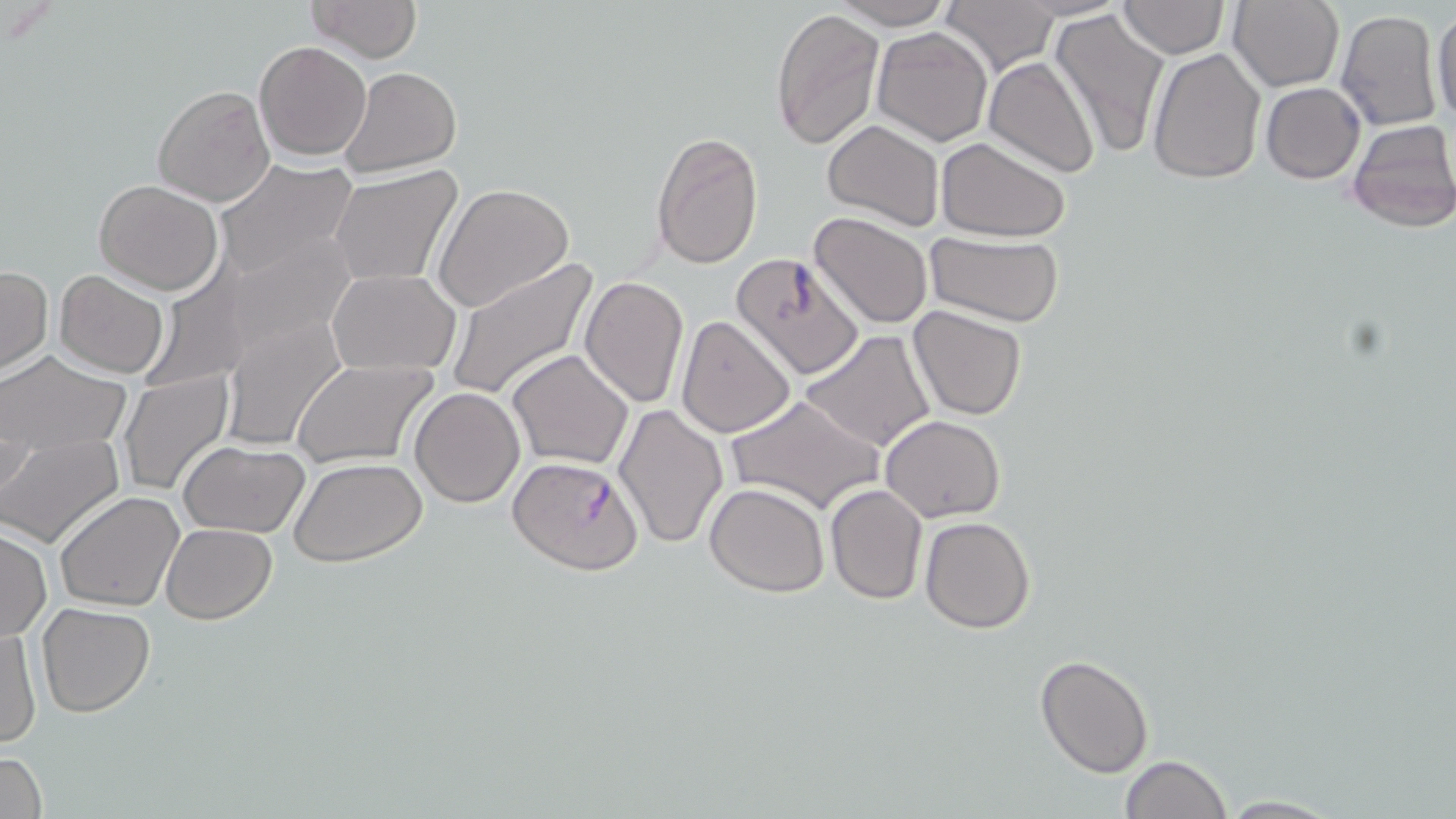 Approximate bounding boxes as (x1,y1)-(x2,y2) corner pairs in pixels. Uninfected red blood cell locations: (304,0)-(422,63), (938,0)-(1061,77), (1011,0)-(1129,20), (1227,0)-(1344,93), (831,1)-(956,29), (1116,1)-(1229,60), (1432,6)-(1456,129), (771,7)-(883,149), (1049,8)-(1168,159), (1335,9)-(1445,132), (871,26)-(994,146), (254,40)-(372,161), (1147,45)-(1267,183), (984,56)-(1101,178), (339,65)-(462,177), (1261,82)-(1365,183), (152,83)-(274,206), (1345,118)-(1456,234), (822,120)-(945,234), (650,130)-(762,270), (936,135)-(1072,241), (212,160)-(359,280), (328,166)-(462,289), (94,179)-(222,294), (433,183)-(575,314), (807,212)-(934,330), (925,231)-(1066,326), (731,251)-(866,382), (445,259)-(600,400), (0,267)-(53,375), (327,267)-(459,374), (54,270)-(169,378), (578,275)-(688,409), (907,305)-(1030,421), (218,315)-(343,450), (675,315)-(796,438), (800,330)-(937,454), (0,349)-(128,451), (507,349)-(634,470), (293,357)-(439,467), (118,370)-(234,496), (410,387)-(525,509), (725,393)-(885,515), (612,401)-(726,550), (879,414)-(1005,522), (0,436)-(121,548), (178,440)-(311,539), (289,458)-(426,568), (705,482)-(830,598), (825,483)-(930,604), (54,491)-(186,611), (919,516)-(1036,634), (160,523)-(276,624), (1,526)-(52,642), (36,603)-(156,716), (1,625)-(41,750), (1034,655)-(1154,777), (0,751)-(47,819), (1119,755)-(1234,818), (1210,794)-(1345,817). Plasmodium falciparum-infected red blood cell locations: (508,455)-(642,575). Slide-level diagnosis: Plasmodium falciparum. May-Grünwald-Giemsa stain. Single field of view. Light microscopy. Thin blood smear. Image is 1456×819 pixels. Captured at 1000x magnification.